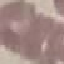
Malaria status: uninfected. Thin smear of blood. Acquired by smartphone through the microscope eyepiece. Automatically extracted cell patch, resized to 64 × 64 pixels. Giemsa-stained preparation.